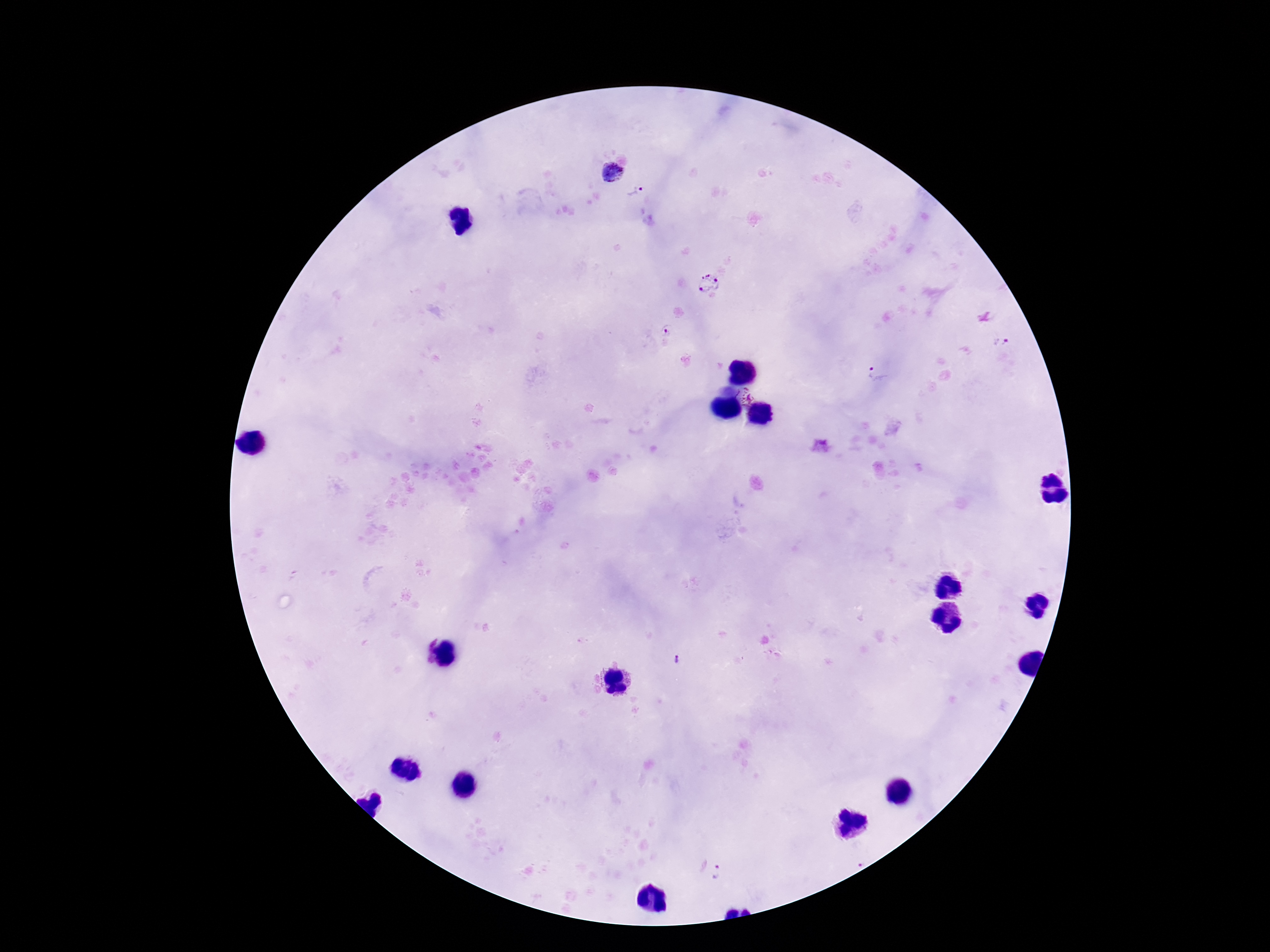

Approximate object centers, in pixels from the top-left corner. Plasmodium parasite locations: (x=611, y=173), (x=636, y=191), (x=708, y=285), (x=666, y=330), (x=1005, y=342), (x=878, y=373), (x=745, y=395), (x=677, y=660), (x=721, y=872). Photographed through the microscope eyepiece with a smartphone camera. Thick blood film. Image is 1270×952 pixels. Patient malaria status: infected. One field from this slide. 100x magnification. Giemsa stain.